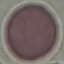
Malaria status: uninfected. Cell patch, automatically extracted from a larger field of view and resized to 64 × 64 pixels. Acquired by smartphone through the microscope eyepiece. Giemsa-stained preparation. Thin smear of blood.